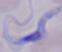

Summary:
  - Identification: trypanosome
  - Magnification: 1000x
  - Modality: micrograph